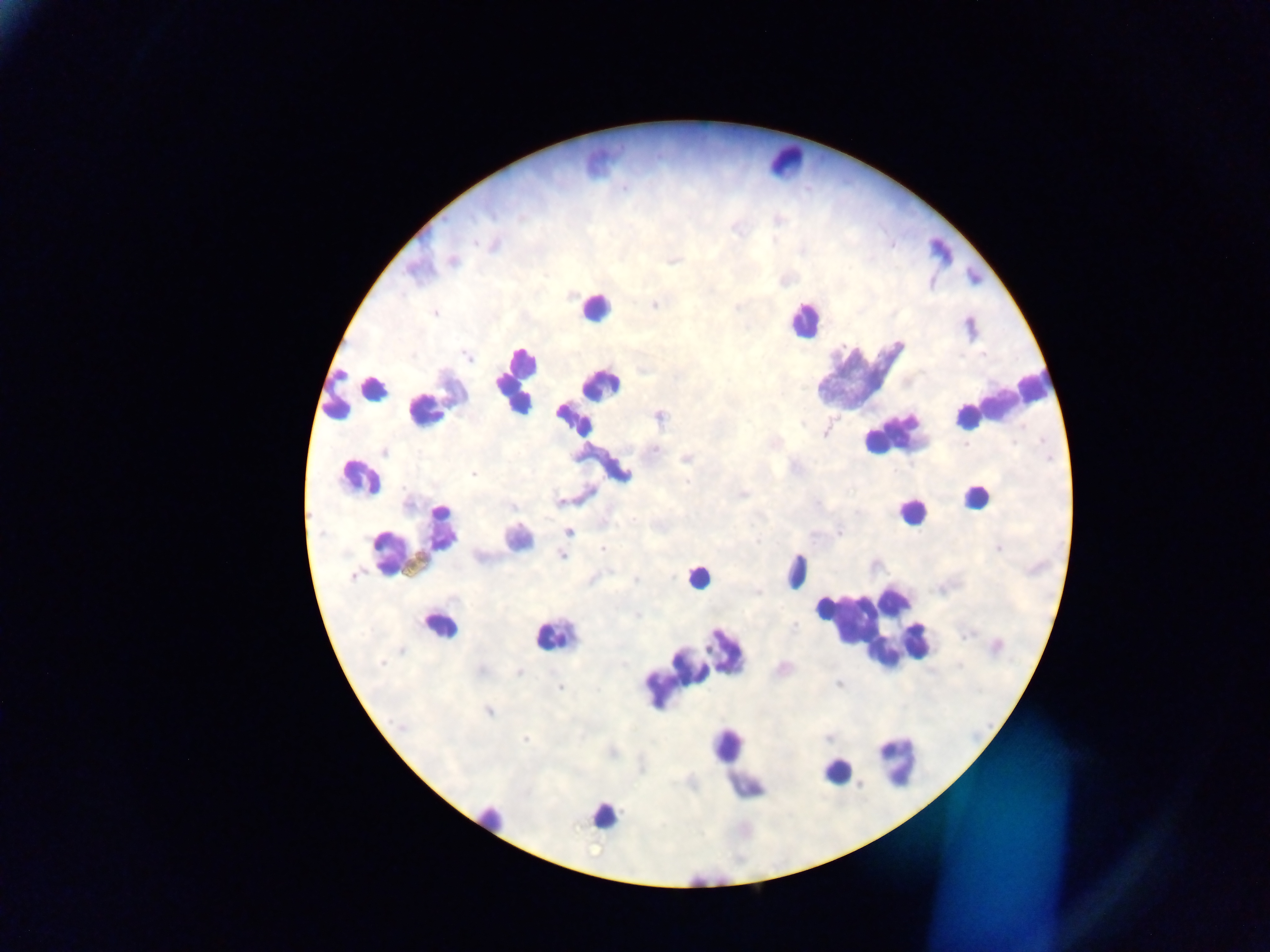
field of view = single
preparation = thick blood smear
country = Ghana
capture = mobile-phone photograph through a microscope
leukocyte locations = approximate centers as x y in pixels: 780 166; 595 313; 800 323; 516 382; 856 386; 355 391; 592 399; 996 404; 356 478; 979 496; 902 519; 417 540; 696 574; 796 575; 439 628; 873 631; 549 635; 688 671; 897 754; 738 772; 838 779; 613 809
Plasmodium parasite locations = approximate centers as x y in pixels: 559 501; 569 532; 603 550; 561 555; 353 577; 560 688; 527 740
image size = 1270×952 pixels